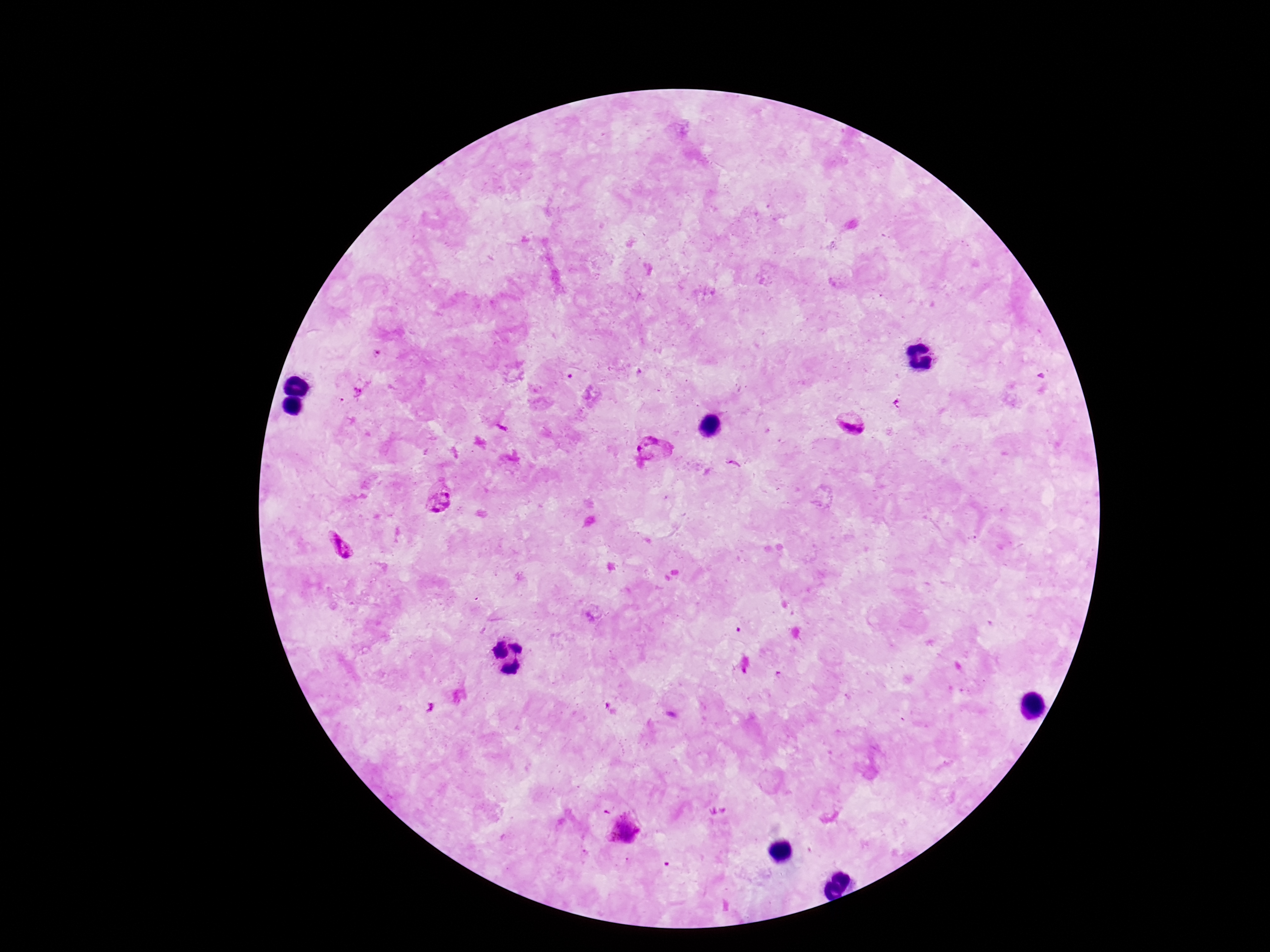 Approximate object centers, in pixels from the top-left corner. Plasmodium parasite locations: (x=851, y=422), (x=655, y=448), (x=438, y=497), (x=340, y=547), (x=623, y=830). Image is 1270×952 pixels. 100x magnification. Smartphone photograph taken through the microscope eyepiece. Giemsa-stained preparation. Patient malaria status: infected. Thick blood film. One field from this slide.